Classify this cell by malaria status.
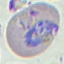
Parasitized.

Giemsa-stained preparation. Thin blood smear. Acquired by smartphone through the microscope eyepiece. Cell patch, automatically extracted from a larger field of view and resized to 64 × 64 pixels.